Name the blood parasite species.
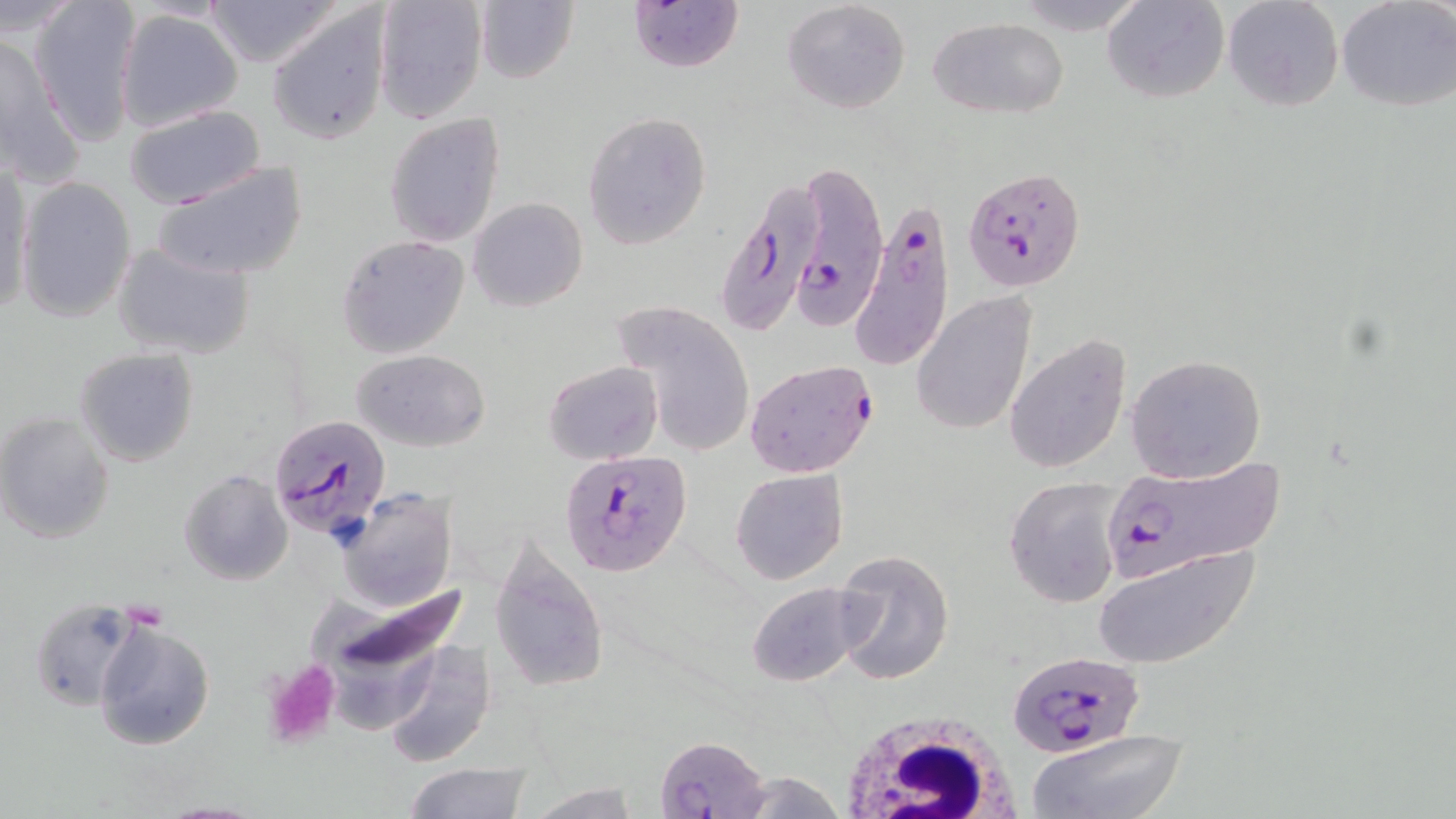
Plasmodium falciparum.

platelet locations = approximate bounding boxes as [x1, y1, x2, y2] in pixels: [259, 658, 343, 750]
magnification = 1000x
uninfected red blood cell locations (subset) = approximate bounding boxes as [x1, y1, x2, y2] in pixels: [28, 0, 142, 146], [198, 0, 347, 70], [372, 0, 487, 124], [624, 0, 743, 73], [781, 0, 910, 114], [1105, 0, 1227, 104], [1222, 0, 1343, 112], [1337, 0, 1455, 111], [472, 1, 579, 84], [267, 4, 393, 146], [114, 7, 244, 133], [929, 15, 1069, 118], [1, 30, 82, 182], [123, 105, 265, 208], [581, 110, 713, 250], [383, 113, 506, 248], [151, 160, 310, 284], [1, 161, 33, 319], [15, 176, 138, 323], [468, 198, 588, 313], [336, 234, 470, 358], [110, 240, 255, 362], [911, 291, 1037, 434], [614, 302, 754, 459], [1004, 333, 1131, 474], [74, 347, 199, 467], [353, 349, 490, 452], [1124, 354, 1267, 483], [542, 361, 663, 464], [0, 412, 116, 544], [178, 469, 293, 586], [731, 469, 848, 585], [1003, 476, 1124, 608], [333, 487, 457, 613], [488, 530, 611, 695], [1093, 543, 1261, 667], [832, 549, 953, 686], [303, 576, 480, 709], [744, 582, 874, 688], [27, 596, 146, 712], [94, 617, 216, 752], [383, 640, 497, 768], [1029, 730, 1189, 819], [400, 764, 533, 818], [522, 781, 642, 817], [149, 801, 272, 818]
stain = May-Grünwald-Giemsa
image size = 1456×819 pixels
white blood cell locations = approximate bounding boxes as [x1, y1, x2, y2] in pixels: [830, 706, 1028, 817]
Plasmodium falciparum-infected red blood cell locations (subset) = approximate bounding boxes as [x1, y1, x2, y2] in pixels: [786, 158, 888, 332], [963, 166, 1088, 291], [721, 177, 828, 334], [858, 204, 956, 366], [744, 359, 879, 478], [268, 412, 394, 538], [561, 449, 693, 576], [1096, 457, 1288, 585], [657, 735, 765, 817]
preparation = thin blood smear
modality = light microscopy
field of view = one of a larger specimen